Identify the blood parasite species.
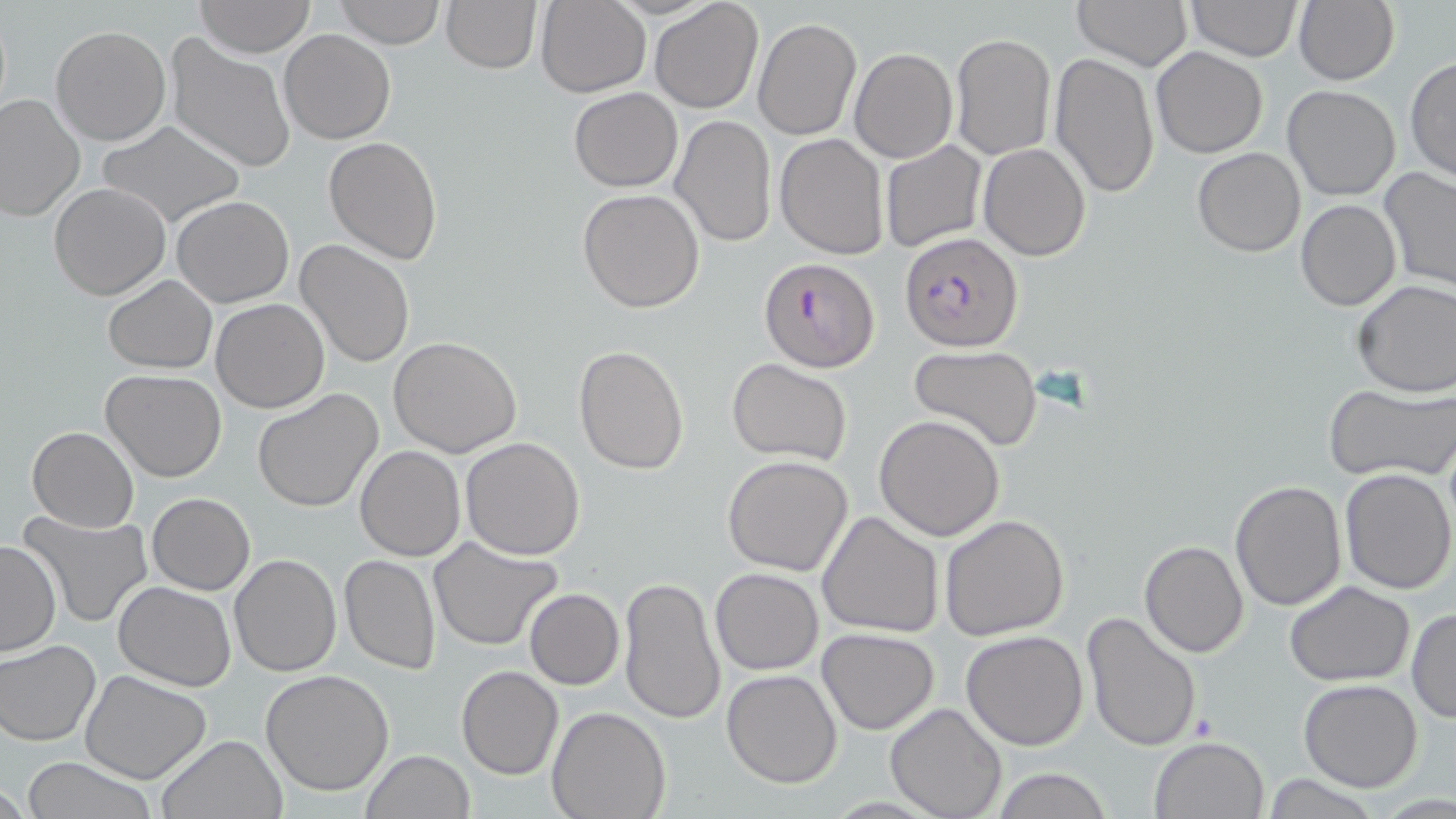

Plasmodium falciparum.

image_size: 1456×819 pixels
plasmodium_falciparum_infected_red_blood_cell_locations: 'approximate bounding boxes as (x1,y1)-(x2,y2) corner pairs in pixels: (899,234)-(1024,351), (758,257)-(879,372)'
modality: light microscopy
field_of_view: one of a larger specimen
uninfected_red_blood_cell_locations: 'approximate bounding boxes as (x1,y1)-(x2,y2) corner pairs in pixels: (332,0)-(445,48), (441,0)-(540,73), (649,0)-(763,114), (1072,0)-(1194,71), (1186,0)-(1303,62), (1293,0)-(1400,86), (195,1)-(315,56), (535,1)-(652,98), (753,17)-(861,139), (50,24)-(172,146), (279,30)-(396,145), (950,32)-(1056,161), (165,34)-(297,175), (1151,47)-(1268,160), (850,48)-(958,164), (1049,52)-(1160,198), (1405,56)-(1456,185), (1282,84)-(1401,201), (568,88)-(682,191), (0,93)-(86,224), (669,114)-(777,249), (96,121)-(246,227), (775,133)-(889,259), (323,136)-(445,264), (879,141)-(987,252), (979,143)-(1091,260), (1193,146)-(1305,256), (1379,168)-(1456,296), (48,183)-(170,300), (577,188)-(706,313), (173,195)-(293,307), (1296,200)-(1401,311), (296,238)-(416,370), (102,274)-(216,374), (1352,280)-(1456,399), (212,298)-(329,413), (389,337)-(522,458), (909,343)-(1042,452), (572,344)-(689,476), (727,360)-(852,464), (101,368)-(227,483), (1322,383)-(1455,483), (251,388)-(385,514), (873,413)-(1005,541), (26,426)-(140,532), (460,437)-(585,558), (355,446)-(465,562), (721,455)-(854,575), (1337,468)-(1455,594), (1229,480)-(1347,612), (147,493)-(254,595), (17,510)-(155,627), (817,510)-(945,640), (940,515)-(1071,642), (428,536)-(564,650), (1139,540)-(1249,657), (0,541)-(61,657), (229,554)-(342,676), (338,554)-(440,674), (710,568)-(824,676), (619,578)-(726,724), (1284,580)-(1416,686), (113,581)-(237,690), (524,588)-(624,690), (1406,606)-(1455,723), (1081,610)-(1202,750), (816,628)-(940,733), (961,631)-(1090,751), (1,639)-(100,747), (456,665)-(563,779), (80,670)-(214,784), (260,670)-(394,796), (722,670)-(843,788), (1298,679)-(1423,792), (886,702)-(1006,819), (546,704)-(672,819), (156,732)-(289,819), (1149,734)-(1270,819), (359,750)-(475,819), (22,756)-(160,819), (990,768)-(1113,819)'
preparation: thin blood smear
magnification: 1000x
stain: May-Grünwald-Giemsa